Give the position of every Plasmodium parasite visible.
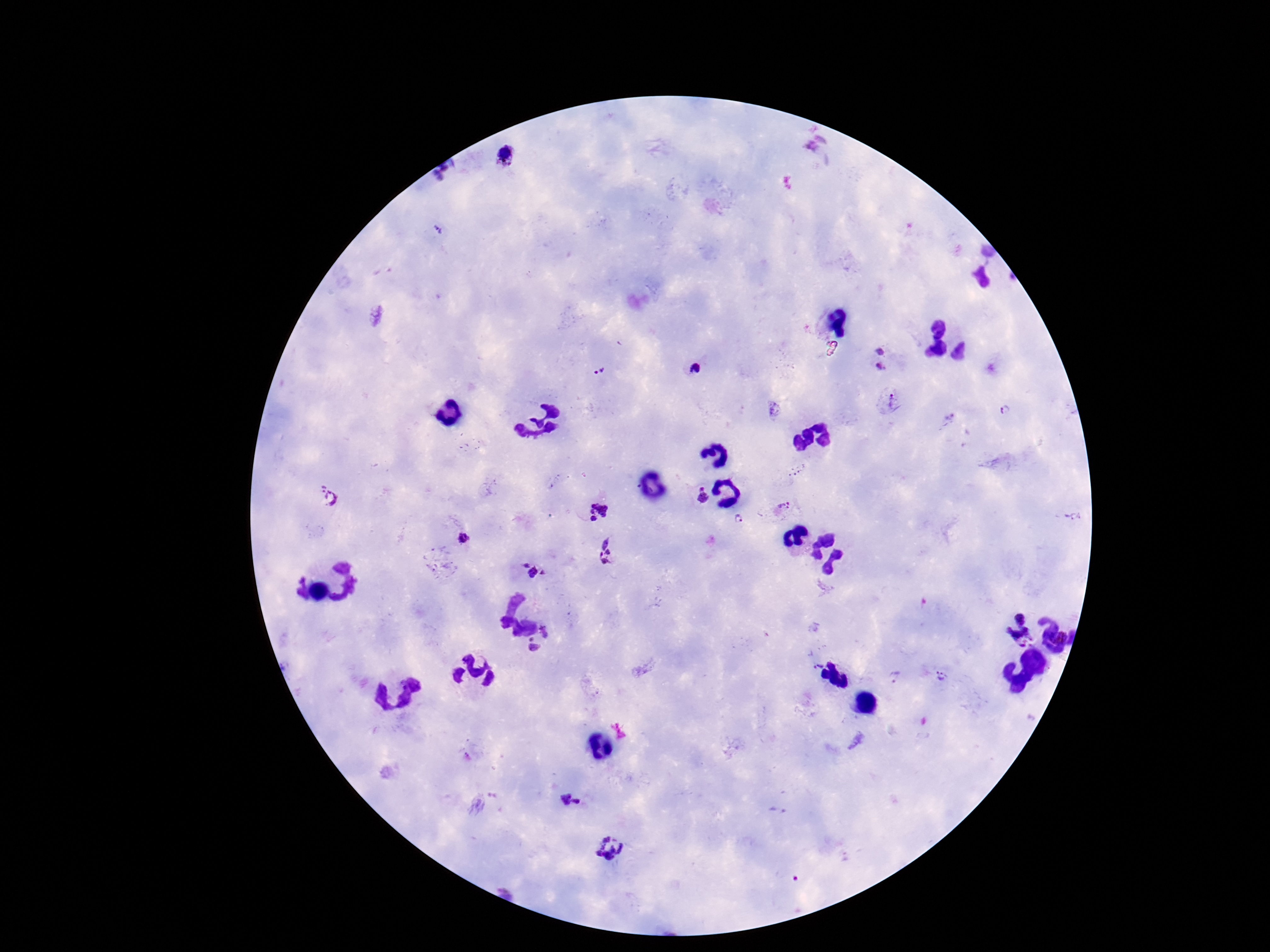
Approximate object centers, in pixels from the top-left corner.
Plasmodium parasites: (x=812, y=145), (x=508, y=155), (x=439, y=230), (x=881, y=348), (x=881, y=367), (x=694, y=369), (x=597, y=370), (x=895, y=399), (x=1005, y=408), (x=774, y=409), (x=703, y=496), (x=327, y=499), (x=784, y=507), (x=598, y=510), (x=1074, y=515), (x=737, y=517), (x=462, y=537), (x=606, y=553), (x=533, y=570), (x=1017, y=627), (x=548, y=632), (x=532, y=648), (x=815, y=664), (x=894, y=676), (x=941, y=677), (x=571, y=801), (x=777, y=809), (x=611, y=846).

Giemsa stain. Smartphone photograph taken through the microscope eyepiece. Image is 1270×952 pixels. Thick blood film. One field from this slide. 100x magnification. Patient malaria status: positive.